Identify the parasite.
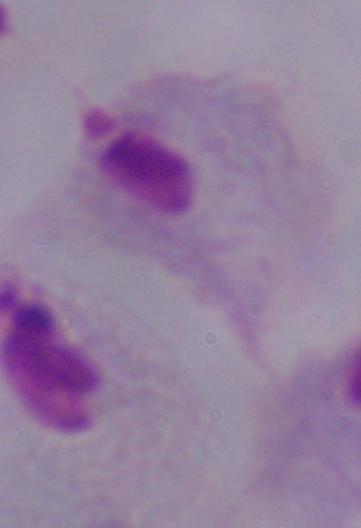

This is a trichomonad.

Micrograph. Captured at 1000x magnification.